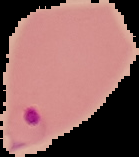
Summary:
  - Preparation: thin blood film
  - Image type: segmented cell region on a black background
  - Malaria status: parasitized
  - Image size: 139×157 pixels